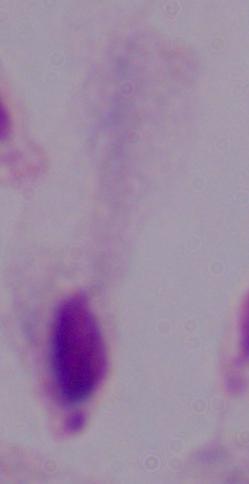
Captured at 1000x magnification. Photomicrograph. A trichomonad is seen.